State which parasite is depicted.
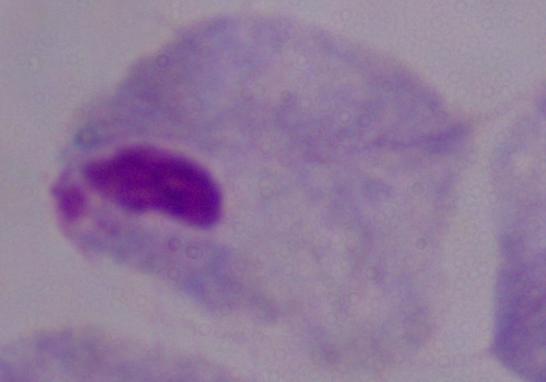

This is a trichomonad.

modality = photomicrograph
magnification = 1000x